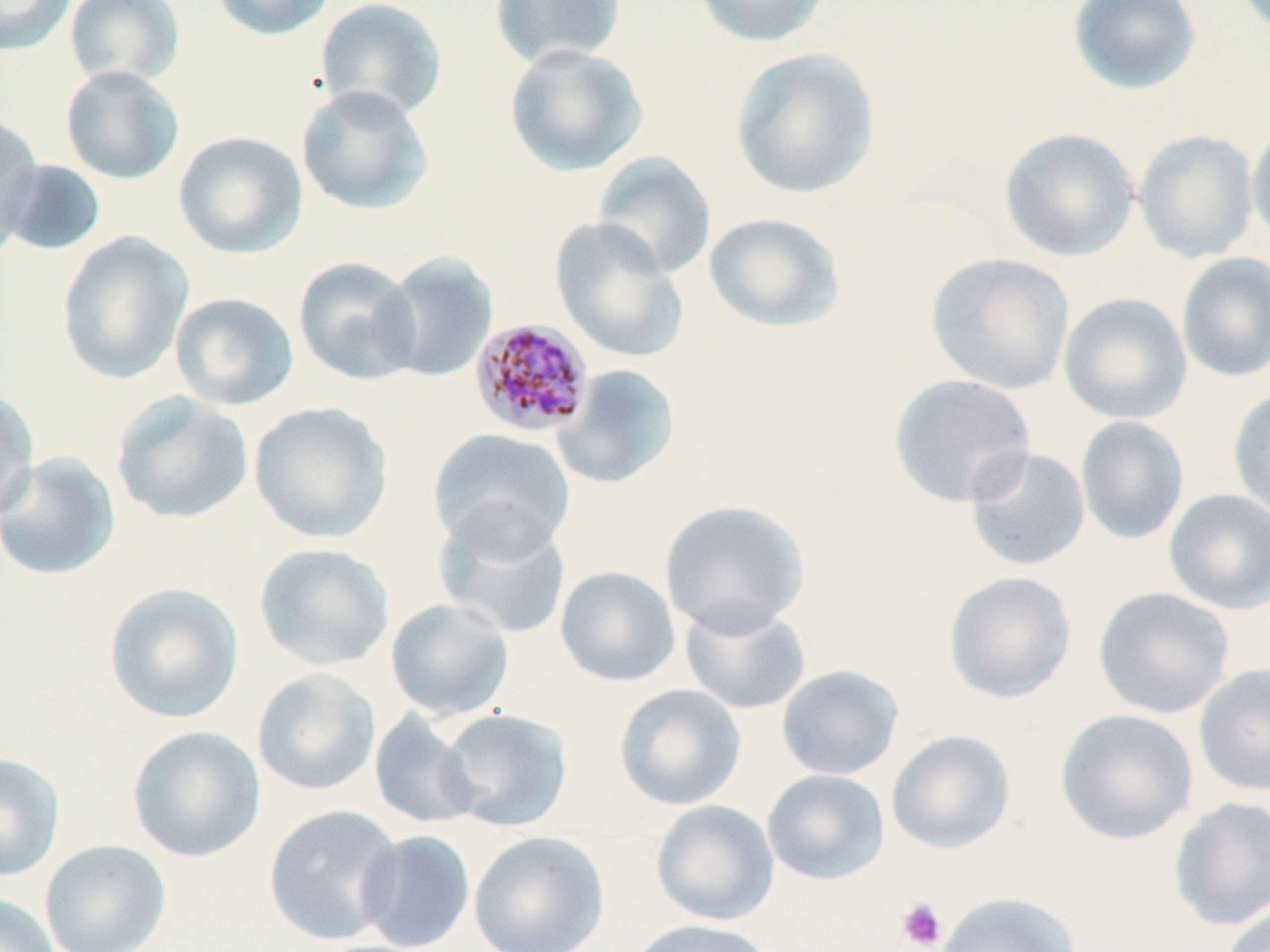 Approximate bounding boxes as named x1/y1/x2/y2 corners in pixels. Plasmodium malariae-infected red blood cell locations: (x1=468, y1=317, x2=594, y2=437). Platelet locations: (x1=897, y1=897, x2=948, y2=951). Uninfected red blood cell locations: (x1=0, y1=0, x2=77, y2=56), (x1=64, y1=0, x2=185, y2=88), (x1=210, y1=0, x2=337, y2=42), (x1=315, y1=0, x2=448, y2=122), (x1=489, y1=0, x2=627, y2=69), (x1=690, y1=0, x2=833, y2=48), (x1=1067, y1=1, x2=1202, y2=95), (x1=503, y1=42, x2=648, y2=177), (x1=730, y1=46, x2=880, y2=200), (x1=60, y1=65, x2=185, y2=186), (x1=295, y1=84, x2=434, y2=216), (x1=0, y1=114, x2=45, y2=254), (x1=1246, y1=122, x2=1270, y2=250), (x1=999, y1=127, x2=1139, y2=261), (x1=1133, y1=129, x2=1259, y2=264), (x1=173, y1=131, x2=309, y2=260), (x1=592, y1=152, x2=717, y2=280), (x1=1, y1=159, x2=107, y2=257), (x1=703, y1=212, x2=846, y2=333), (x1=550, y1=218, x2=687, y2=362), (x1=55, y1=232, x2=194, y2=384), (x1=376, y1=252, x2=499, y2=381), (x1=1176, y1=252, x2=1270, y2=383), (x1=926, y1=253, x2=1075, y2=396), (x1=293, y1=256, x2=422, y2=385), (x1=169, y1=292, x2=300, y2=412), (x1=1058, y1=293, x2=1192, y2=424), (x1=553, y1=364, x2=681, y2=490), (x1=889, y1=373, x2=1038, y2=509), (x1=0, y1=387, x2=40, y2=522), (x1=1227, y1=388, x2=1270, y2=524), (x1=111, y1=391, x2=253, y2=525), (x1=249, y1=401, x2=394, y2=544), (x1=1075, y1=415, x2=1190, y2=545), (x1=427, y1=428, x2=576, y2=557), (x1=965, y1=446, x2=1091, y2=572), (x1=0, y1=451, x2=121, y2=581), (x1=1163, y1=488, x2=1270, y2=615), (x1=659, y1=499, x2=811, y2=636), (x1=433, y1=504, x2=573, y2=641), (x1=253, y1=543, x2=395, y2=671), (x1=555, y1=565, x2=681, y2=687), (x1=943, y1=571, x2=1077, y2=704), (x1=102, y1=582, x2=244, y2=724), (x1=1093, y1=586, x2=1235, y2=719), (x1=385, y1=597, x2=515, y2=722), (x1=680, y1=601, x2=812, y2=715), (x1=1193, y1=662, x2=1270, y2=798), (x1=777, y1=664, x2=904, y2=781), (x1=252, y1=668, x2=381, y2=796), (x1=613, y1=683, x2=747, y2=811), (x1=437, y1=708, x2=574, y2=832), (x1=1055, y1=708, x2=1199, y2=845), (x1=369, y1=710, x2=483, y2=830), (x1=126, y1=726, x2=265, y2=863), (x1=886, y1=730, x2=1016, y2=854), (x1=0, y1=752, x2=67, y2=882), (x1=762, y1=769, x2=890, y2=885), (x1=1168, y1=796, x2=1270, y2=931), (x1=650, y1=799, x2=780, y2=926), (x1=263, y1=804, x2=404, y2=946), (x1=354, y1=829, x2=476, y2=951), (x1=468, y1=831, x2=610, y2=952), (x1=39, y1=839, x2=171, y2=952), (x1=935, y1=890, x2=1081, y2=952), (x1=0, y1=893, x2=61, y2=952), (x1=1220, y1=902, x2=1270, y2=952), (x1=623, y1=919, x2=779, y2=952). Slide-level diagnosis: Plasmodium malariae. 1000x magnification. Image is 1270×952 pixels. Thin blood smear. Single field of view. May-Grünwald-Giemsa stain. Light microscopy.